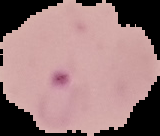 Result: Plasmodium parasites detected. Image is 160×136 pixels. Segmented cell region on a black background. From a thin blood film.